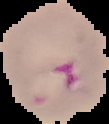

preparation = thin blood smear
image size = 109×124 pixels
malaria status = parasitized
image type = cell region segmented out of the field of view; surrounding area masked to black